Report the malaria status.
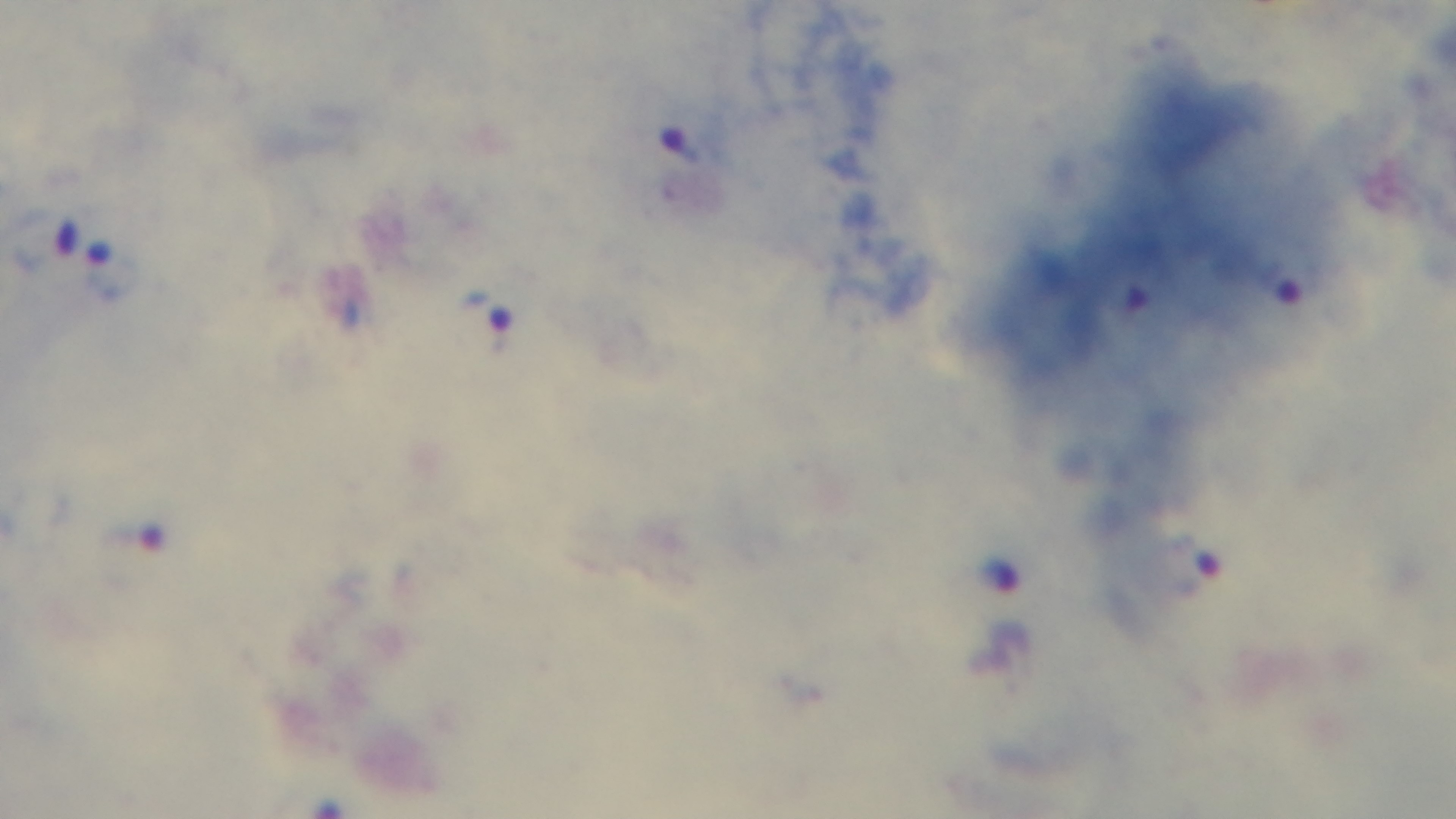
Positive.

stain = Giemsa
capture = mounted 4K digital camera
modality = light microscopy
field of view = one from the slide
preparation = thick
objective = 100x oil immersion